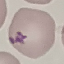 Result: no malaria parasites detected. Thin blood film. Giemsa stain. Automatically extracted cell patch, resized to 64 × 64 pixels. Acquired by smartphone through the microscope eyepiece.